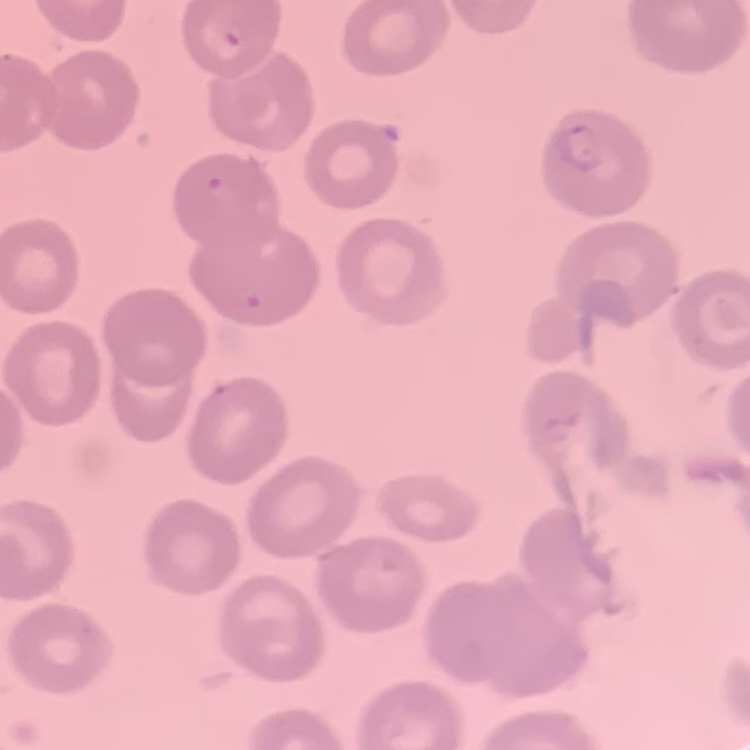
Summary:
  - Red blood cell morphology: no rouleaux formation
  - Image type: square crop of a larger photomicrograph
  - Preparation: thin peripheral smear
  - Stain: Field's or Giemsa